Assess for Plasmodium parasites.
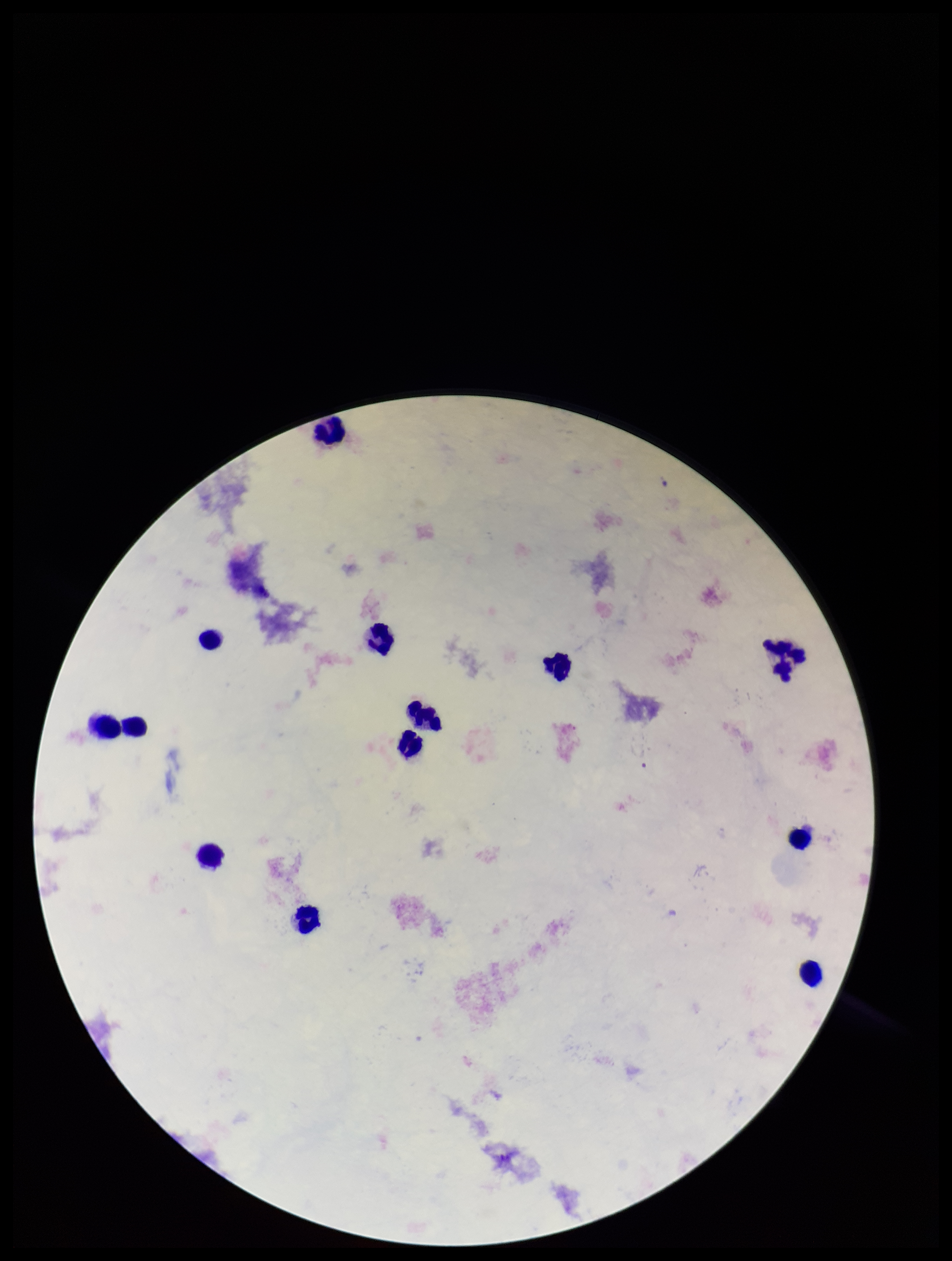

None identified.

preparation = thick smear
leukocyte count = 13
capture = smartphone photograph through the microscope eyepiece
image size = 952×1261 pixels
patient malaria status = negative
parasite count = 0
field of view = single
stain = Giemsa